Give the position of every leukocyte visible.
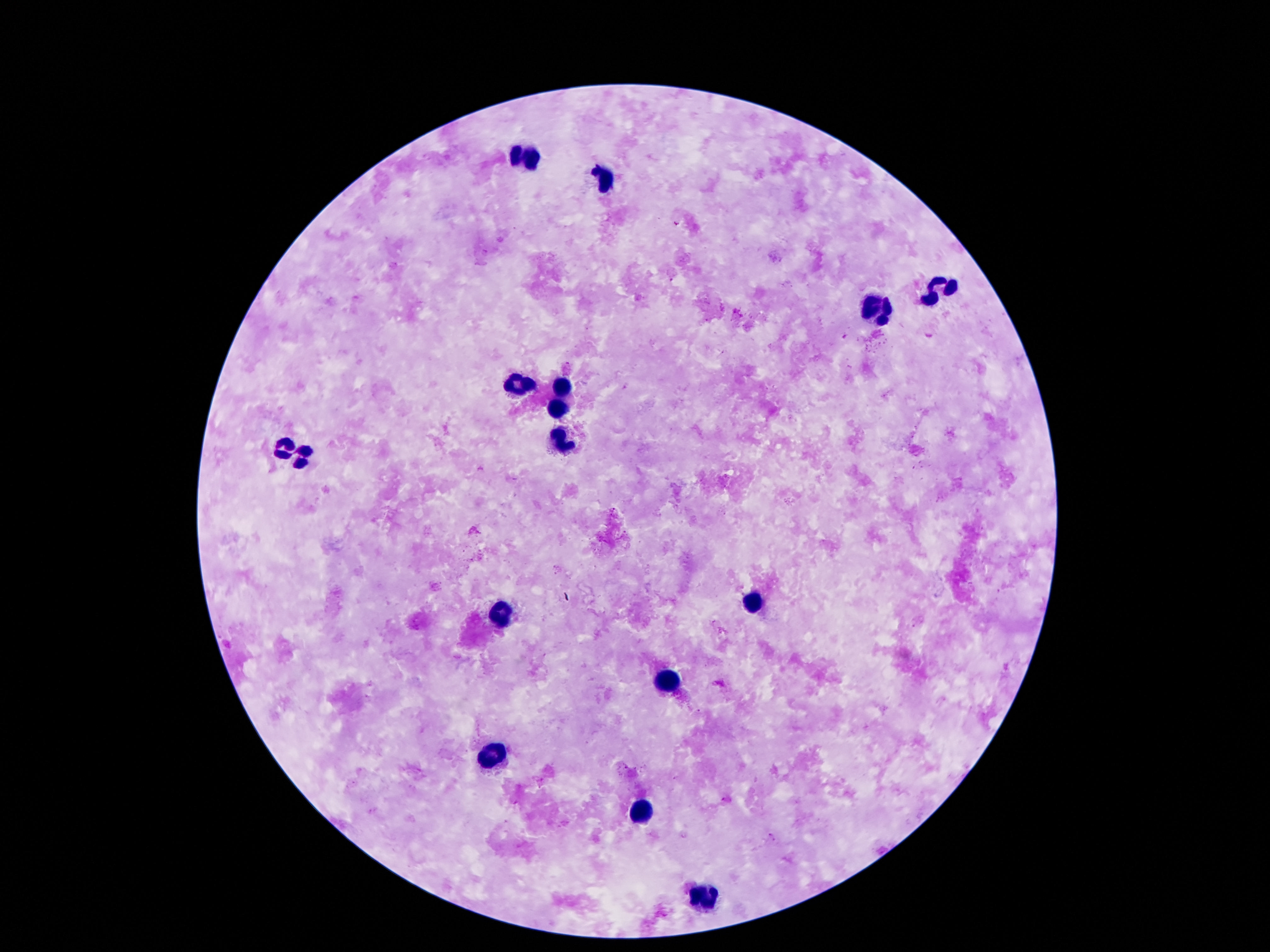
Approximate centers as {x, y} in pixels.
Leukocytes: {522, 155}, {602, 180}, {940, 288}, {881, 309}, {562, 388}, {517, 390}, {557, 405}, {564, 441}, {289, 449}, {749, 603}, {502, 610}, {669, 679}, {492, 754}, {642, 810}, {707, 897}.

One field from this slide. Image is 1270×952 pixels. Patient malaria status: negative. 100x magnification. Smartphone photograph taken through the microscope eyepiece. Giemsa-stained preparation. Thick blood film.